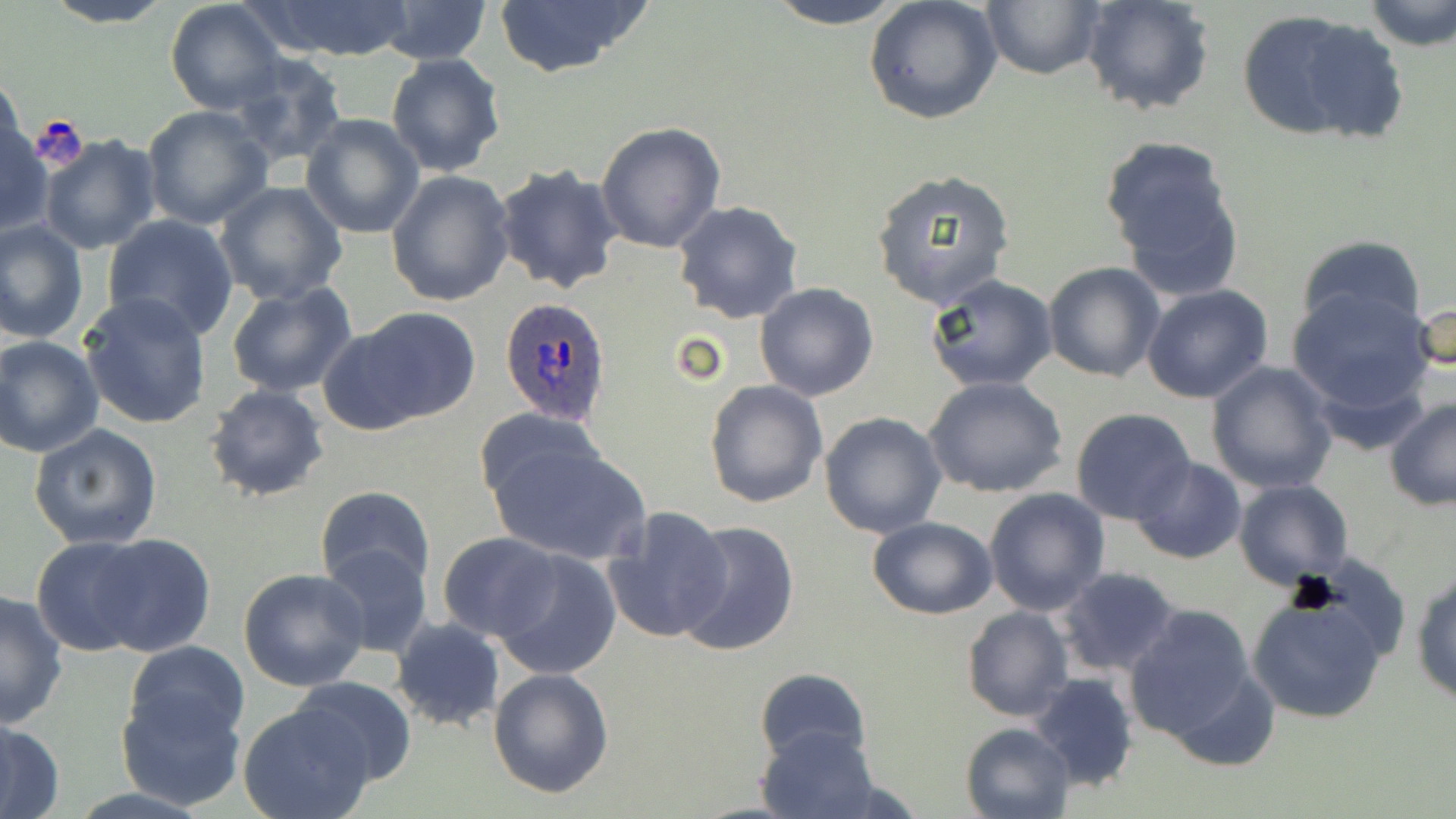
plasmodium_ovale_infected_red_blood_cell_locations: 'approximate bounding boxes as named x1/y1/x2/y2 corners in pixels: (x1=500, y1=296, x2=613, y2=427)'
slide_level_diagnosis: Plasmodium ovale
stain: May-Grünwald-Giemsa
preparation: thin blood film
modality: optical microscopy
magnification: 1000x
image_size: 1456×819 pixels
uninfected_red_blood_cell_locations: 'approximate bounding boxes as named x1/y1/x2/y2 corners in pixels: (x1=41, y1=0, x2=173, y2=28), (x1=489, y1=0, x2=653, y2=79), (x1=760, y1=0, x2=913, y2=26), (x1=864, y1=0, x2=1003, y2=125), (x1=1080, y1=0, x2=1215, y2=117), (x1=1361, y1=0, x2=1455, y2=51), (x1=252, y1=1, x2=417, y2=63), (x1=165, y1=2, x2=289, y2=116), (x1=980, y1=2, x2=1104, y2=81), (x1=370, y1=3, x2=497, y2=64), (x1=1235, y1=9, x2=1404, y2=147), (x1=385, y1=52, x2=507, y2=176), (x1=229, y1=53, x2=349, y2=168), (x1=0, y1=71, x2=27, y2=172), (x1=142, y1=105, x2=272, y2=229), (x1=300, y1=114, x2=425, y2=239), (x1=0, y1=119, x2=50, y2=236), (x1=597, y1=122, x2=726, y2=252), (x1=37, y1=133, x2=163, y2=256), (x1=1100, y1=137, x2=1246, y2=299), (x1=492, y1=164, x2=624, y2=294), (x1=870, y1=169, x2=1016, y2=311), (x1=386, y1=170, x2=513, y2=307), (x1=215, y1=181, x2=348, y2=304), (x1=672, y1=199, x2=804, y2=323), (x1=102, y1=214, x2=238, y2=339), (x1=0, y1=218, x2=89, y2=347), (x1=1296, y1=235, x2=1426, y2=340), (x1=1043, y1=263, x2=1166, y2=382), (x1=924, y1=272, x2=1058, y2=391), (x1=226, y1=280, x2=357, y2=398), (x1=754, y1=282, x2=879, y2=401), (x1=1141, y1=284, x2=1275, y2=403), (x1=1288, y1=287, x2=1436, y2=426), (x1=78, y1=291, x2=212, y2=431), (x1=1410, y1=298, x2=1455, y2=378), (x1=342, y1=307, x2=484, y2=428), (x1=0, y1=335, x2=104, y2=458), (x1=1206, y1=362, x2=1339, y2=493), (x1=926, y1=378, x2=1067, y2=498), (x1=703, y1=379, x2=828, y2=509), (x1=202, y1=383, x2=329, y2=502), (x1=706, y1=398, x2=943, y2=524), (x1=1384, y1=399, x2=1456, y2=510), (x1=472, y1=406, x2=609, y2=518), (x1=1070, y1=409, x2=1197, y2=525), (x1=818, y1=412, x2=947, y2=537), (x1=29, y1=422, x2=163, y2=550), (x1=488, y1=437, x2=650, y2=564), (x1=1129, y1=456, x2=1247, y2=565), (x1=1234, y1=480, x2=1352, y2=588), (x1=315, y1=485, x2=436, y2=594), (x1=984, y1=486, x2=1110, y2=615), (x1=602, y1=505, x2=734, y2=644), (x1=866, y1=516, x2=997, y2=619), (x1=674, y1=519, x2=800, y2=657), (x1=437, y1=531, x2=562, y2=642), (x1=90, y1=533, x2=215, y2=657), (x1=30, y1=537, x2=157, y2=655), (x1=318, y1=541, x2=434, y2=659), (x1=492, y1=549, x2=621, y2=679), (x1=237, y1=567, x2=371, y2=691), (x1=1056, y1=567, x2=1182, y2=678), (x1=1412, y1=567, x2=1456, y2=705), (x1=1247, y1=588, x2=1393, y2=724), (x1=0, y1=590, x2=69, y2=727), (x1=1121, y1=604, x2=1266, y2=748), (x1=960, y1=606, x2=1072, y2=722), (x1=390, y1=618, x2=505, y2=733), (x1=124, y1=640, x2=250, y2=748), (x1=488, y1=667, x2=615, y2=798), (x1=755, y1=667, x2=870, y2=767), (x1=1028, y1=672, x2=1138, y2=793), (x1=290, y1=675, x2=417, y2=786), (x1=114, y1=686, x2=248, y2=811), (x1=238, y1=701, x2=381, y2=819), (x1=0, y1=717, x2=66, y2=818), (x1=960, y1=721, x2=1077, y2=818), (x1=757, y1=724, x2=879, y2=819)'
field_of_view: one of a larger specimen